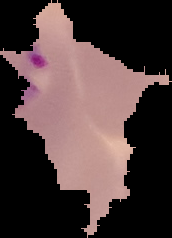

Segmented cell region on a black background. Malaria status: parasitized. Image is 172×238 pixels. From a thin blood smear.